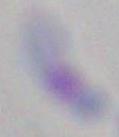

modality: photomicrograph
magnification: 1000x
identification: Toxoplasma gondii